Outline each uninfected red blood cell.
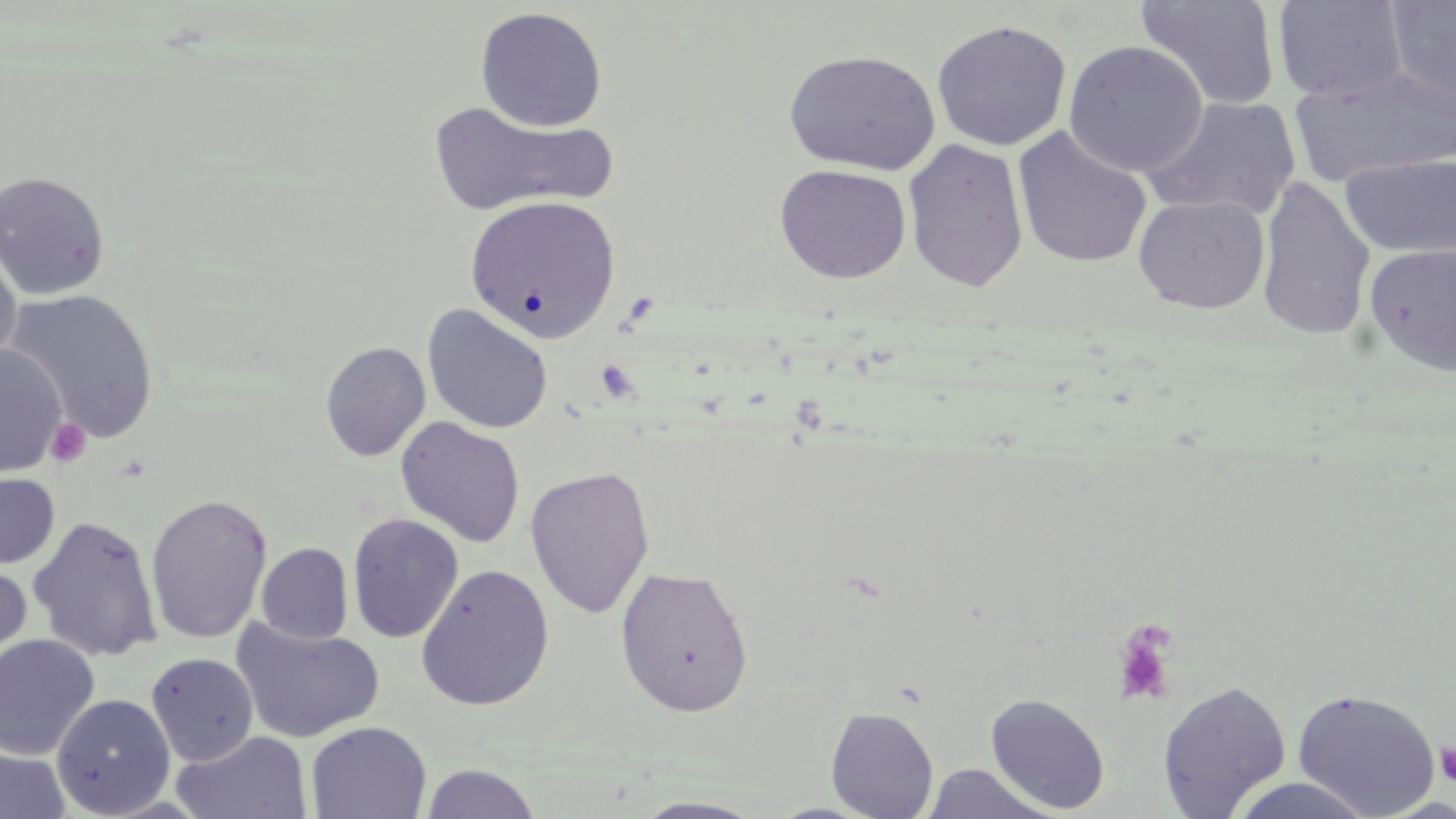
Approximate bounding boxes as [x1, y1, x2, y2] in pixels.
Uninfected red blood cells: [1272, 0, 1409, 104], [1384, 0, 1456, 106], [1135, 1, 1282, 111], [474, 6, 608, 132], [931, 19, 1072, 152], [1063, 40, 1207, 177], [783, 50, 941, 176], [1289, 65, 1454, 188], [1142, 96, 1303, 221], [427, 99, 615, 218], [1012, 126, 1152, 269], [902, 138, 1029, 292], [1340, 152, 1456, 260], [774, 163, 911, 283], [0, 170, 111, 300], [1255, 175, 1376, 342], [463, 194, 620, 344], [1133, 194, 1271, 314], [1364, 242, 1456, 376], [0, 246, 22, 375], [5, 289, 160, 442], [422, 304, 553, 434], [320, 341, 431, 462], [0, 344, 67, 480], [395, 416, 525, 548], [524, 465, 655, 619], [0, 472, 60, 570], [146, 493, 272, 644], [347, 512, 464, 644], [27, 515, 163, 662], [256, 543, 353, 644], [0, 558, 33, 683], [415, 563, 555, 711], [615, 565, 753, 717], [230, 618, 385, 744], [0, 634, 100, 760], [146, 652, 259, 766], [1157, 680, 1292, 818], [1291, 687, 1442, 817], [51, 693, 175, 817], [985, 693, 1111, 814], [825, 706, 939, 819], [305, 721, 432, 818], [172, 730, 312, 819], [0, 745, 71, 819], [921, 763, 1057, 819], [419, 764, 543, 819], [1228, 776, 1378, 819], [630, 797, 769, 819].

Summary:
  - Platelet locations: [47, 419, 91, 467], [1110, 620, 1179, 706], [1434, 741, 1456, 788]
  - Slide-level diagnosis: no evidence of blood parasites
  - Image size: 1456×819 pixels
  - Modality: optical microscopy
  - Preparation: thin blood smear
  - Stain: May-Grünwald-Giemsa
  - Magnification: 1000x
  - Field of view: one of a larger specimen